Locate every Plasmodium ovale-infected red blood cell.
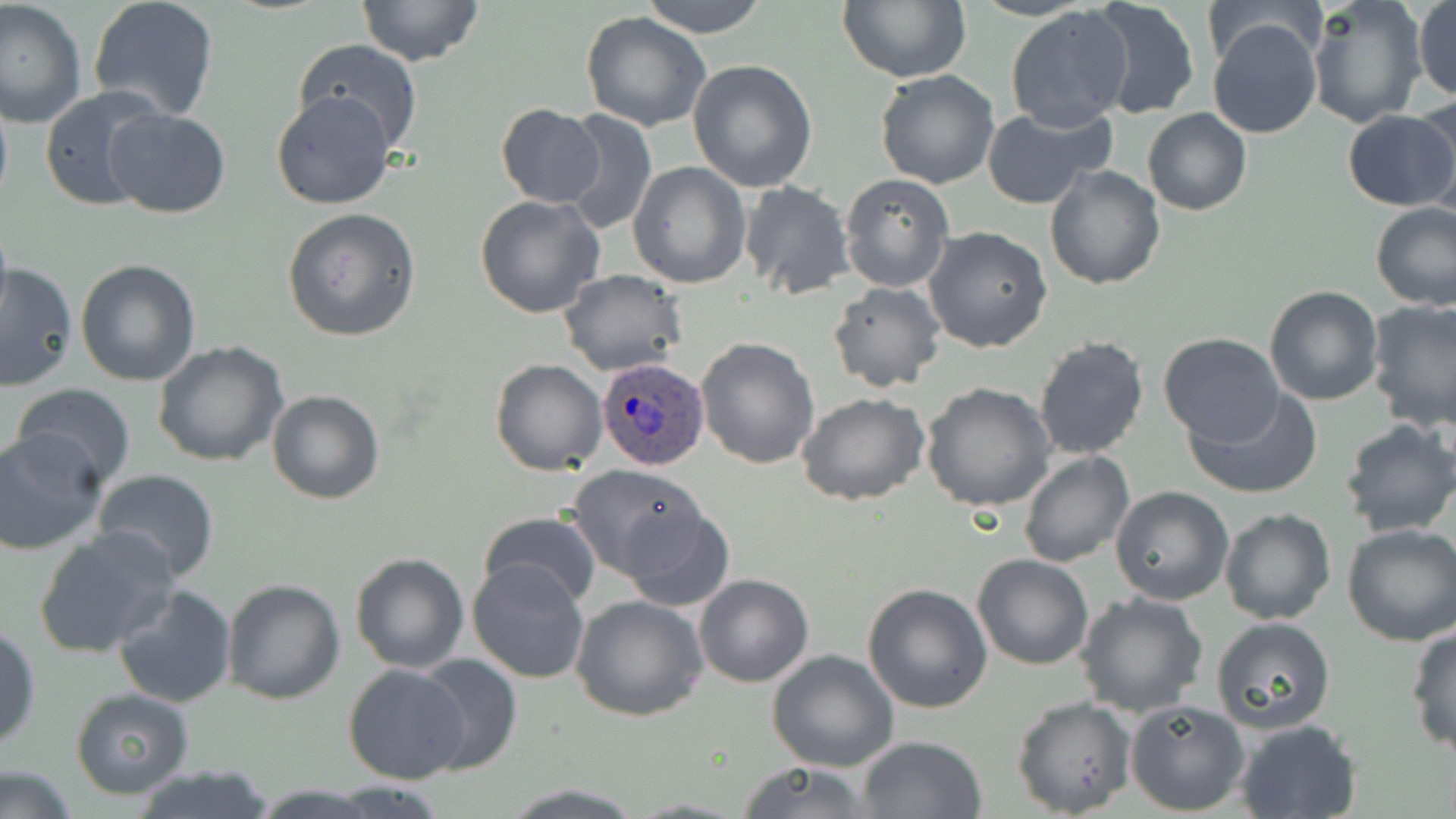

Approximate bounding boxes as (x1,y1)-(x2,y2) corner pairs in pixels.
Plasmodium ovale-infected red blood cells: (593,359)-(709,470).

slide-level diagnosis = Plasmodium ovale
magnification = 1000x
preparation = thin blood smear
stain = May-Grünwald-Giemsa
image size = 1456×819 pixels
field of view = one of a larger specimen
modality = light microscopy
uninfected red blood cell locations = approximate bounding boxes as (x1,y1)-(x2,y2) corner pairs in pixels: (87,0)-(220,122), (357,0)-(485,67), (639,0)-(768,38), (837,0)-(969,83), (1087,0)-(1202,122), (1307,0)-(1427,130), (1413,0)-(1456,104), (1,1)-(86,132), (1202,2)-(1325,69), (1004,6)-(1133,132), (581,10)-(712,132), (1207,17)-(1323,140), (291,38)-(424,155), (688,60)-(819,193), (875,70)-(1001,189), (0,84)-(12,217), (40,86)-(169,212), (270,90)-(397,210), (1411,97)-(1456,218), (497,105)-(604,206), (981,105)-(1113,208), (1143,107)-(1251,216), (104,108)-(230,219), (558,109)-(657,235), (1342,109)-(1456,212), (628,161)-(751,289), (1043,165)-(1166,290), (840,175)-(953,292), (739,181)-(855,299), (475,194)-(606,318), (1371,203)-(1455,311), (282,208)-(420,341), (0,218)-(13,324), (923,226)-(1053,354), (76,260)-(202,386), (0,261)-(77,393), (560,269)-(687,377), (827,281)-(945,393), (1263,284)-(1383,405), (1365,299)-(1456,432), (1158,331)-(1286,446), (1033,334)-(1148,461), (695,337)-(820,469), (152,340)-(289,468), (490,358)-(606,475), (921,382)-(1055,512), (10,383)-(135,491), (1186,387)-(1321,500), (266,389)-(385,506), (797,393)-(929,507), (1337,418)-(1456,537), (0,430)-(104,555), (1019,450)-(1135,569), (567,464)-(709,580), (91,468)-(220,581), (1111,485)-(1234,605), (618,504)-(737,611), (1219,508)-(1337,626), (476,509)-(603,609), (1341,524)-(1456,646), (34,526)-(180,660), (350,553)-(469,673), (971,555)-(1095,671), (468,557)-(593,684), (694,573)-(814,689), (222,578)-(345,703), (862,582)-(993,713), (112,583)-(238,707), (1075,593)-(1207,718), (573,594)-(707,720), (1210,616)-(1337,735), (1405,623)-(1456,757), (0,626)-(40,751), (766,651)-(899,772), (411,653)-(523,775), (343,664)-(472,784), (70,689)-(195,799), (1012,696)-(1136,817), (1125,698)-(1250,816), (1235,719)-(1362,819), (857,735)-(987,819), (0,761)-(79,819), (733,762)-(879,818), (128,765)-(280,819), (499,781)-(642,816)